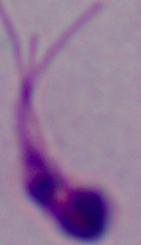

Captured at 1000x magnification. A Leishmania parasite is shown. Micrograph.